Identify the parasite.
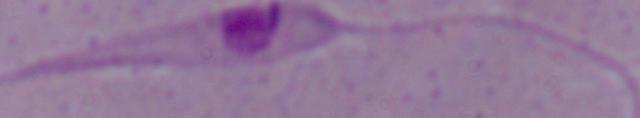

Leishmania.

magnification = 1000x
modality = micrograph